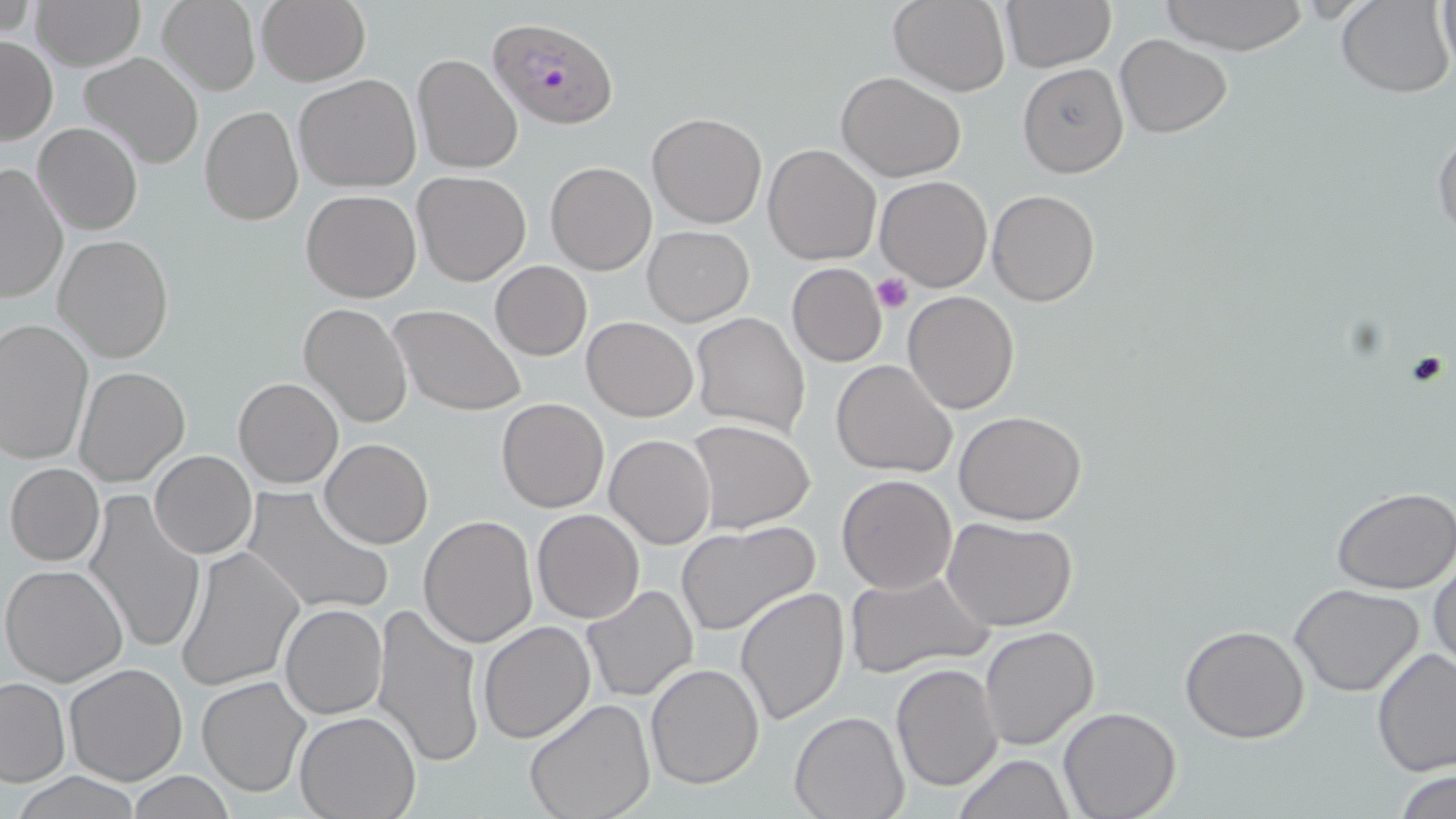

{
  "slide_level_diagnosis": "Plasmodium falciparum",
  "uninfected_red_blood_cell_locations": "approximate bounding boxes as [x1, y1, x2, y2] in pixels: [29, 0, 145, 69], [888, 0, 1012, 95], [999, 0, 1116, 72], [1156, 0, 1308, 53], [1434, 0, 1455, 77], [157, 1, 260, 95], [255, 1, 370, 86], [1335, 1, 1455, 98], [1, 35, 57, 142], [1114, 35, 1232, 139], [79, 51, 205, 169], [412, 53, 523, 174], [1018, 63, 1128, 177], [836, 70, 968, 182], [294, 73, 422, 191], [199, 104, 304, 227], [646, 111, 767, 228], [34, 121, 142, 235], [1433, 125, 1456, 244], [763, 143, 882, 266], [544, 162, 657, 275], [1, 164, 68, 303], [413, 170, 532, 285], [876, 175, 993, 291], [301, 189, 421, 303], [987, 189, 1100, 307], [642, 225, 755, 326], [54, 235, 173, 362], [489, 260, 592, 361], [787, 263, 887, 366], [903, 291, 1020, 414], [297, 302, 413, 429], [391, 304, 526, 417], [691, 312, 811, 437], [581, 316, 698, 421], [0, 319, 95, 464], [832, 359, 958, 477], [74, 366, 190, 487], [233, 376, 344, 488], [496, 397, 610, 513], [954, 410, 1088, 525], [686, 419, 816, 533], [605, 433, 716, 549], [321, 437, 433, 549], [150, 450, 256, 558], [5, 463, 104, 565], [836, 474, 957, 593], [240, 486, 394, 619], [1332, 488, 1456, 594], [84, 489, 208, 658], [531, 509, 644, 624], [419, 515, 538, 649], [942, 517, 1078, 632], [675, 521, 820, 636], [175, 546, 305, 690], [1431, 553, 1455, 677], [1, 562, 129, 686], [843, 569, 994, 677], [580, 584, 699, 703], [1290, 584, 1424, 696], [736, 586, 850, 726], [371, 602, 486, 769], [280, 604, 388, 719], [479, 620, 596, 742], [1180, 624, 1310, 744], [980, 626, 1101, 751], [1371, 648, 1456, 778], [891, 661, 1004, 794], [64, 663, 188, 786], [646, 663, 764, 789], [197, 674, 312, 798], [1, 676, 69, 785], [524, 699, 657, 819], [1059, 706, 1181, 819], [789, 709, 908, 819], [294, 712, 420, 819], [953, 753, 1075, 819], [1395, 768, 1456, 819], [13, 772, 146, 819], [126, 772, 237, 816]",
  "field_of_view": "one of a larger specimen",
  "stain": "May-Grünwald-Giemsa",
  "preparation": "thin blood film",
  "modality": "optical microscopy",
  "image_size": "1456×819 pixels",
  "platelet_locations": "approximate bounding boxes as [x1, y1, x2, y2] in pixels: [873, 274, 913, 314], [1405, 350, 1448, 390]",
  "plasmodium_falciparum_infected_red_blood_cell_locations": "approximate bounding boxes as [x1, y1, x2, y2] in pixels: [489, 17, 620, 130]",
  "magnification": "1000x"
}